Outline each blood parasite and name the species.
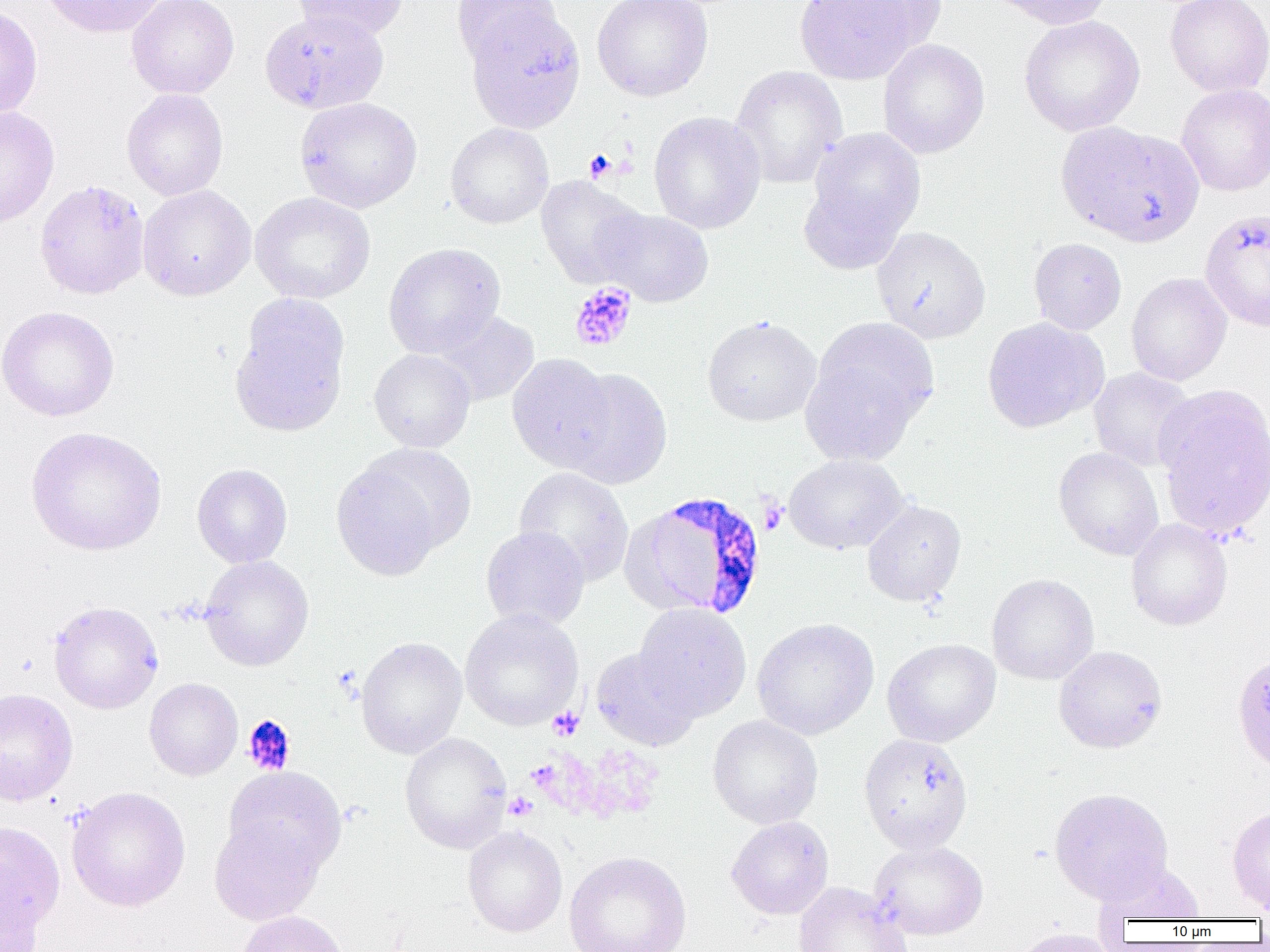

Approximate bounding boxes as (x1,y1)-(x2,y2) corner pairs in pixels.
Plasmodium falciparum-infected red blood cells: (636,492)-(768,619).
No Plasmodium ovale, Plasmodium malariae, Plasmodium vivax, Babesia divergens, or Trypanosoma brucei observed.

slide_level_diagnosis: Plasmodium falciparum
image_size: 1270×952 pixels
uninfected_red_blood_cell_locations: 'approximate bounding boxes as (x1,y1)-(x2,y2) corner pairs in pixels: (40,0)-(171,38), (126,0)-(239,99), (291,0)-(408,42), (451,0)-(562,68), (592,0)-(713,101), (794,0)-(926,85), (842,0)-(947,52), (985,0)-(1115,29), (1164,0)-(1270,97), (0,3)-(44,120), (465,7)-(586,133), (260,9)-(389,114), (1018,15)-(1145,136), (878,39)-(990,159), (729,65)-(848,190), (1176,83)-(1270,197), (121,88)-(228,201), (294,97)-(423,213), (0,105)-(60,227), (648,111)-(766,234), (1056,121)-(1203,247), (445,122)-(554,229), (805,127)-(925,257), (536,175)-(649,288), (137,185)-(257,301), (250,192)-(375,304), (596,207)-(714,307), (872,226)-(991,344), (1029,238)-(1127,335), (383,243)-(505,359), (1126,272)-(1232,386), (230,294)-(351,437), (0,305)-(119,422), (434,310)-(539,406), (701,316)-(821,426), (981,317)-(1108,433), (799,340)-(930,466), (369,348)-(476,453), (507,354)-(614,472), (1088,367)-(1196,472), (559,369)-(673,489), (1154,384)-(1270,537), (25,426)-(167,556), (1053,446)-(1164,560), (331,447)-(466,578), (783,454)-(909,554), (192,463)-(292,568), (513,467)-(634,586), (862,500)-(966,606), (1126,518)-(1232,631), (480,526)-(590,631), (199,555)-(313,671), (986,573)-(1099,685), (49,600)-(163,714), (634,603)-(752,721), (459,608)-(583,730), (752,618)-(879,740), (355,636)-(467,758), (882,638)-(1001,747), (1054,645)-(1167,753), (591,647)-(701,751), (1231,651)-(1270,774), (144,678)-(243,781), (0,688)-(78,806), (707,715)-(823,829), (399,732)-(512,853), (858,734)-(973,853), (223,766)-(346,876), (67,787)-(190,912), (1049,788)-(1172,903), (1227,807)-(1270,913), (209,816)-(326,926), (726,816)-(834,920), (0,820)-(65,947), (463,826)-(567,937), (870,840)-(988,941), (564,850)-(692,952), (1092,861)-(1206,924), (0,877)-(45,952), (793,882)-(912,952), (237,910)-(349,952), (1007,928)-(1119,952)'
preparation: thin blood smear
modality: light microscopy
magnification: 1000x
platelet_locations: 'approximate bounding boxes as (x1,y1)-(x2,y2) corner pairs in pixels: (584,150)-(617,182), (570,282)-(637,351), (758,498)-(787,535), (547,707)-(584,741), (242,715)-(296,776), (504,792)-(538,820)'
field_of_view: single